Assess this cell for malaria.
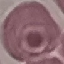
It is uninfected.

{
  "image_type": "cell patch, automatically extracted from a larger field of view and resized to 64 × 64 pixels",
  "preparation": "thin blood smear",
  "stain": "Giemsa",
  "capture": "smartphone through the microscope eyepiece"
}